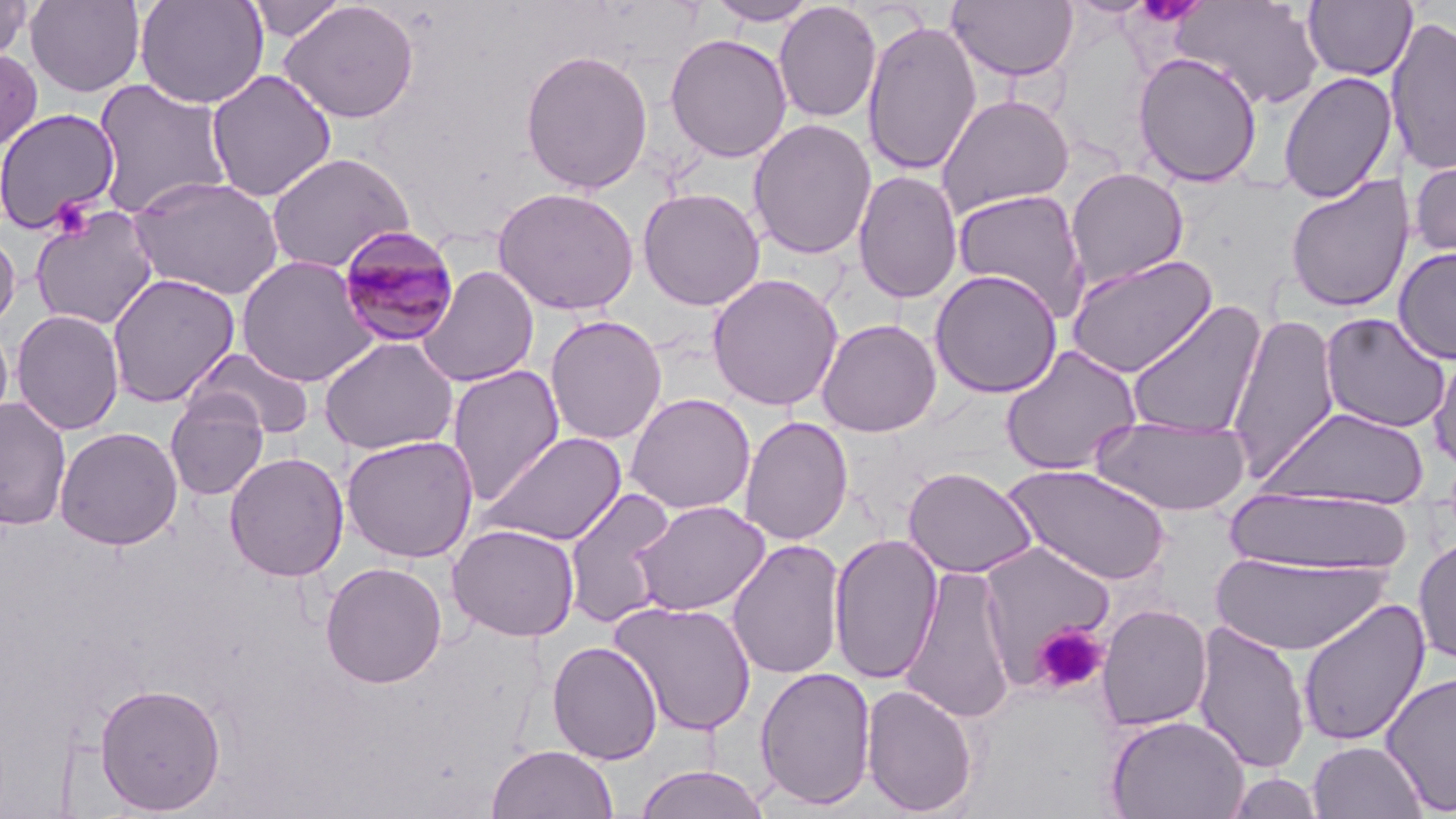
slide-level diagnosis = Plasmodium malariae
magnification = 1000x
stain = May-Grünwald-Giemsa
Plasmodium malariae-infected red blood cell locations = approximate bounding boxes as [x1, y1, x2, y2] in pixels: [334, 225, 461, 350]
uninfected red blood cell locations = approximate bounding boxes as [x1, y1, x2, y2] in pixels: [0, 0, 34, 64], [24, 0, 145, 97], [135, 0, 269, 109], [246, 0, 348, 42], [706, 0, 821, 26], [1173, 0, 1325, 111], [279, 1, 420, 124], [946, 1, 1079, 82], [1302, 1, 1417, 82], [773, 2, 882, 123], [1386, 15, 1456, 177], [861, 19, 982, 176], [665, 33, 793, 163], [0, 47, 43, 154], [519, 48, 654, 194], [1132, 51, 1263, 188], [205, 69, 337, 202], [1278, 71, 1398, 204], [91, 79, 233, 219], [936, 93, 1075, 217], [0, 107, 121, 234], [748, 118, 876, 260], [1409, 147, 1456, 267], [265, 151, 414, 273], [1065, 167, 1189, 289], [852, 169, 963, 304], [1284, 174, 1416, 313], [129, 175, 285, 300], [491, 186, 640, 316], [637, 187, 765, 311], [951, 187, 1090, 321], [30, 205, 159, 330], [0, 226, 21, 332], [1393, 247, 1456, 364], [1064, 253, 1219, 379], [236, 256, 378, 386], [417, 266, 540, 387], [929, 269, 1063, 398], [106, 272, 240, 407], [707, 273, 844, 412], [1125, 300, 1268, 439], [10, 309, 126, 436], [1320, 312, 1451, 433], [1226, 313, 1340, 483], [544, 314, 667, 446], [0, 317, 14, 434], [815, 318, 942, 437], [318, 336, 459, 456], [1000, 344, 1143, 476], [1428, 344, 1456, 474], [186, 346, 315, 439], [447, 364, 564, 506], [624, 392, 756, 515], [164, 393, 269, 500], [0, 397, 71, 530], [1260, 406, 1431, 508], [1091, 413, 1253, 516], [739, 415, 853, 545], [54, 426, 183, 550], [479, 431, 628, 546], [341, 434, 479, 562], [224, 451, 349, 582], [1003, 462, 1172, 586], [902, 466, 1038, 578], [1224, 487, 1415, 575], [562, 488, 678, 628], [629, 500, 771, 617], [447, 523, 580, 642], [828, 532, 943, 685], [1413, 536, 1456, 665], [726, 538, 846, 680], [977, 539, 1118, 684], [1211, 552, 1392, 657], [320, 561, 448, 688], [899, 565, 1018, 725], [1297, 598, 1430, 747], [608, 599, 758, 736], [1096, 603, 1212, 731], [1026, 611, 1113, 695], [1191, 620, 1311, 774], [547, 641, 663, 765], [754, 666, 877, 811], [1380, 670, 1456, 816], [95, 682, 227, 814], [860, 683, 980, 817], [1104, 714, 1250, 819], [1307, 740, 1428, 819], [485, 744, 619, 819], [633, 765, 771, 819], [1223, 772, 1325, 818]
image size = 1456×819 pixels
modality = optical microscopy
preparation = thin blood film
field of view = one of a larger specimen
platelet locations = approximate bounding boxes as [x1, y1, x2, y2] in pixels: [50, 196, 95, 237], [1032, 624, 1108, 695]